State the blood parasite species.
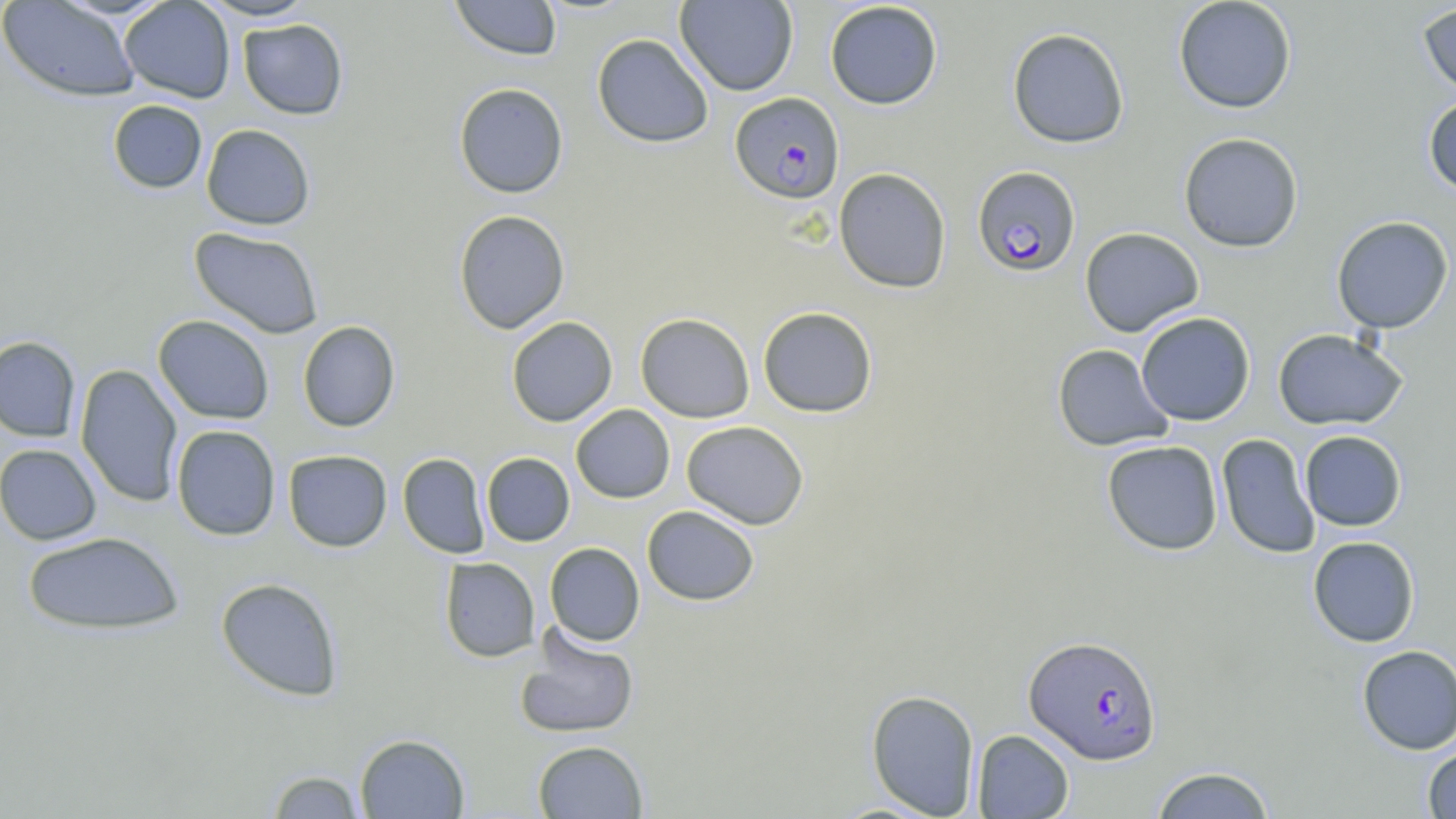
Plasmodium falciparum.

Summary:
  - Coordinate format: approximate bounding boxes as (x1, y1, x2, y2) in pixels
  - Uninfected red blood cell locations: (0, 0, 140, 101), (119, 0, 236, 103), (199, 0, 318, 21), (450, 0, 562, 61), (675, 0, 799, 96), (1173, 0, 1296, 113), (824, 1, 943, 110), (1417, 2, 1456, 101), (238, 18, 349, 120), (1007, 27, 1129, 148), (592, 33, 714, 148), (453, 82, 568, 198), (1423, 95, 1456, 198), (107, 100, 207, 194), (201, 123, 315, 230), (1178, 132, 1304, 252), (833, 167, 952, 293), (453, 209, 571, 334), (1331, 215, 1454, 334), (189, 226, 324, 339), (1079, 227, 1204, 337), (757, 306, 878, 418), (635, 312, 755, 423), (1136, 312, 1256, 426), (153, 315, 275, 424), (507, 316, 618, 426), (297, 320, 400, 432), (1272, 328, 1408, 431), (0, 336, 81, 441), (1052, 343, 1174, 451), (75, 364, 183, 507), (571, 404, 675, 503), (681, 420, 809, 529), (171, 425, 281, 540), (1299, 430, 1407, 531), (1216, 433, 1320, 558), (1102, 440, 1223, 555), (0, 444, 102, 545), (283, 449, 392, 552), (481, 452, 575, 546), (398, 453, 490, 558), (642, 505, 760, 606), (21, 531, 184, 635), (1307, 536, 1420, 647), (544, 542, 645, 646), (439, 557, 541, 662), (215, 577, 344, 701), (514, 629, 639, 739), (1356, 645, 1456, 754), (865, 689, 981, 818), (971, 729, 1074, 818), (354, 733, 470, 818), (533, 740, 648, 818), (1422, 744, 1456, 818), (1149, 766, 1277, 818), (266, 769, 367, 818)
  - Plasmodium falciparum-infected red blood cell locations: (730, 92, 845, 204), (972, 165, 1081, 277), (1023, 635, 1161, 764)
  - Field of view: single
  - Stain: May-Grünwald-Giemsa
  - Preparation: thin blood smear
  - Magnification: 1000x
  - Image size: 1456×819 pixels
  - Modality: optical microscopy